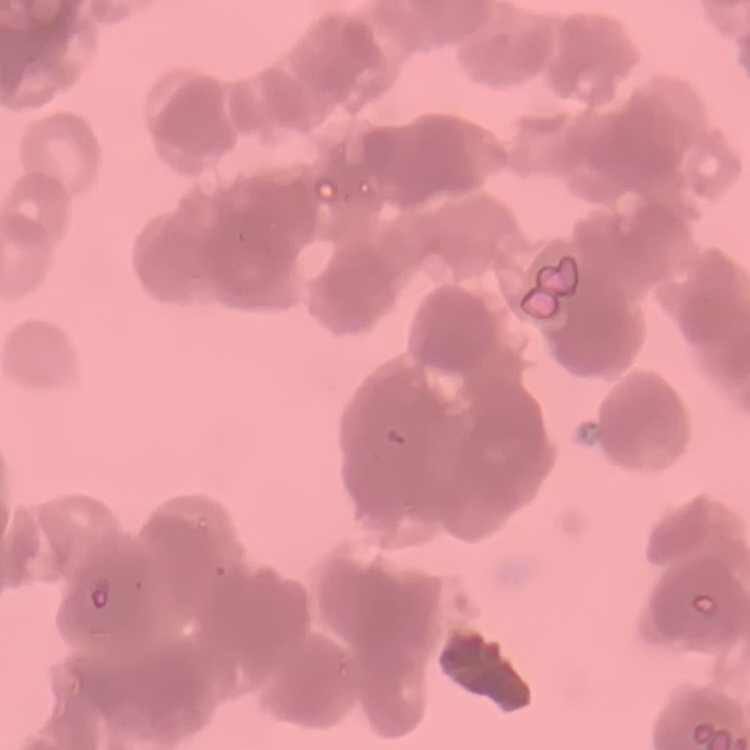
The erythrocytes exhibit rouleaux formation. One tile cut from a larger photomicrograph. Field's or Giemsa stain. Thin blood film.